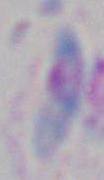

{
  "magnification": "1000x",
  "identification": "Toxoplasma gondii",
  "modality": "micrograph"
}